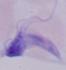

magnification: 1000x
identification: trypanosome
modality: micrograph